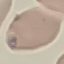

Summary:
  - Result: no malaria parasites seen
  - Image type: cell patch, automatically extracted from a larger field of view and resized to 64 × 64 pixels
  - Preparation: thin blood film
  - Stain: Giemsa
  - Capture: smartphone through the microscope eyepiece